State the blood parasite species.
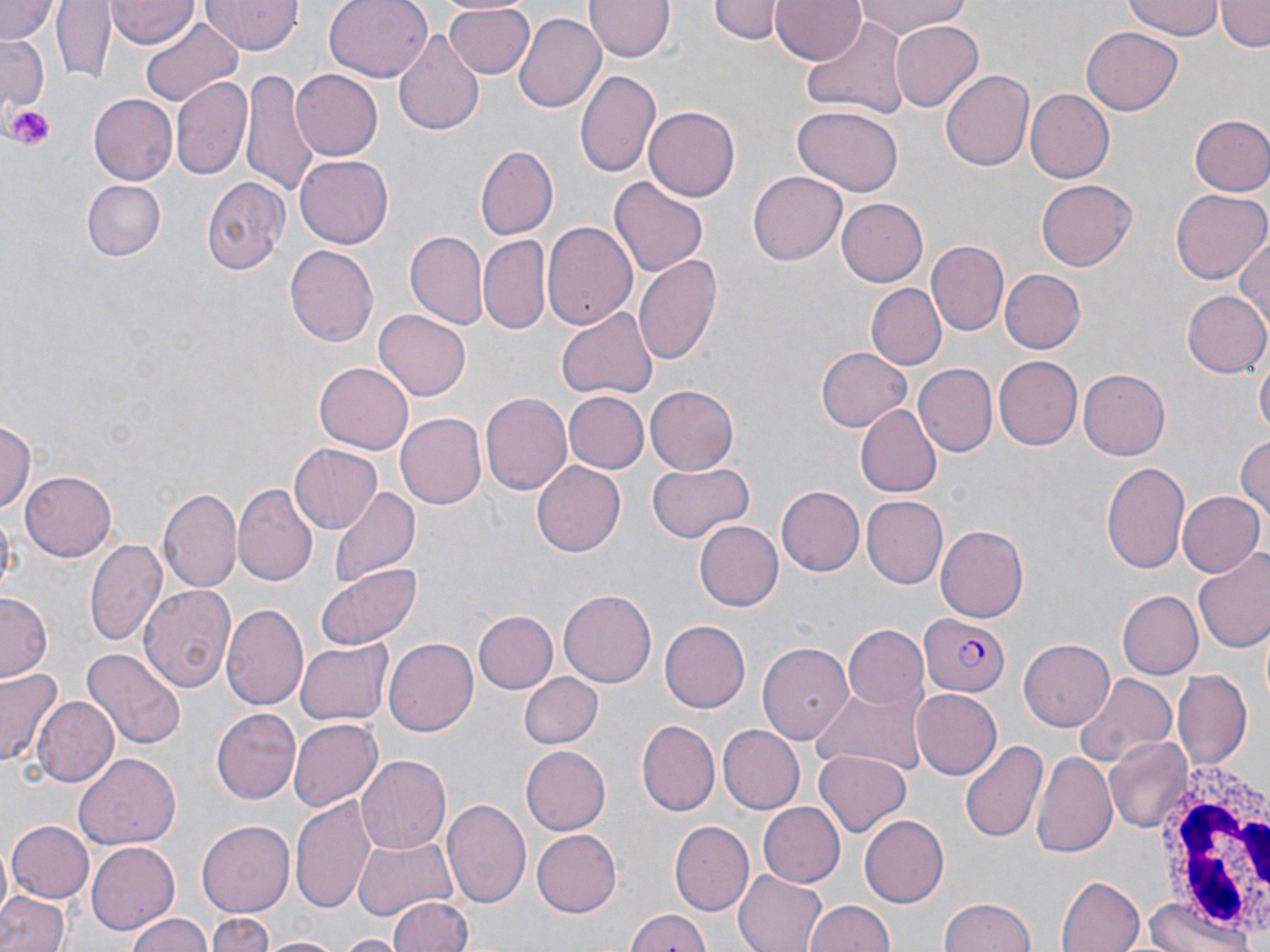
Plasmodium falciparum.

{
  "modality": "light microscopy",
  "white_blood_cell_locations": "approximate bounding boxes as [x1, y1, x2, y2] in pixels: [1149, 755, 1270, 944]",
  "image_size": "1270×952 pixels",
  "preparation": "thin blood film",
  "stain": "May-Grünwald-Giemsa",
  "platelet_locations": "approximate bounding boxes as [x1, y1, x2, y2] in pixels: [6, 103, 56, 148]",
  "magnification": "1000x",
  "field_of_view": "one of a larger specimen",
  "plasmodium_falciparum_infected_red_blood_cell_locations": "approximate bounding boxes as [x1, y1, x2, y2] in pixels: [920, 612, 1012, 698]",
  "uninfected_red_blood_cell_locations": "approximate bounding boxes as [x1, y1, x2, y2] in pixels: [0, 0, 61, 45], [51, 0, 115, 84], [198, 0, 305, 56], [325, 0, 433, 81], [584, 0, 671, 61], [712, 0, 779, 44], [770, 0, 862, 65], [852, 0, 969, 38], [1122, 0, 1224, 40], [1218, 0, 1269, 52], [107, 2, 196, 48], [443, 4, 533, 77], [513, 11, 605, 113], [137, 15, 243, 107], [803, 16, 911, 119], [890, 21, 984, 111], [1083, 26, 1183, 113], [392, 28, 483, 137], [0, 35, 48, 114], [242, 68, 320, 203], [575, 68, 661, 180], [940, 68, 1035, 171], [291, 69, 383, 160], [171, 74, 254, 180], [1025, 89, 1114, 183], [89, 93, 177, 185], [790, 105, 903, 196], [644, 106, 739, 201], [1188, 114, 1270, 198], [476, 146, 558, 240], [295, 155, 392, 248], [748, 172, 846, 265], [202, 175, 290, 276], [610, 176, 707, 276], [1035, 178, 1138, 271], [81, 179, 165, 261], [1170, 189, 1267, 285], [837, 197, 928, 288], [541, 217, 638, 331], [406, 230, 485, 330], [1234, 233, 1269, 340], [479, 236, 550, 333], [927, 241, 1007, 334], [285, 243, 378, 349], [633, 254, 722, 369], [999, 269, 1084, 354], [867, 283, 946, 369], [1182, 291, 1270, 378], [556, 306, 658, 401], [373, 309, 470, 403], [816, 347, 912, 432], [994, 354, 1082, 450], [1256, 355, 1269, 440], [314, 361, 414, 453], [914, 364, 997, 456], [1079, 369, 1170, 460], [645, 385, 738, 473], [480, 391, 573, 495], [565, 392, 649, 474], [854, 404, 941, 499], [396, 414, 485, 509], [0, 417, 35, 518], [1234, 431, 1269, 532], [289, 444, 382, 533], [1100, 459, 1191, 574], [646, 460, 754, 546], [532, 462, 625, 558], [20, 470, 116, 561], [234, 484, 318, 589], [156, 486, 241, 593], [328, 486, 419, 590], [776, 486, 863, 577], [1175, 489, 1263, 579], [862, 496, 948, 587], [693, 519, 782, 611], [936, 524, 1028, 622], [85, 538, 167, 647], [1194, 551, 1270, 656], [315, 563, 422, 650], [138, 583, 237, 692], [558, 588, 657, 688], [1118, 590, 1203, 678], [1, 591, 54, 684], [219, 604, 308, 713], [473, 611, 556, 694], [659, 620, 749, 713], [842, 625, 927, 710], [384, 635, 479, 737], [1021, 638, 1115, 730], [296, 639, 392, 725], [758, 641, 853, 747], [80, 647, 187, 749], [0, 667, 62, 770], [1172, 671, 1252, 771], [517, 672, 603, 750], [1073, 674, 1176, 766], [814, 681, 925, 774], [912, 689, 1002, 779], [31, 695, 118, 789], [212, 708, 300, 804], [289, 718, 383, 811], [637, 720, 718, 816], [718, 723, 806, 813], [1105, 736, 1192, 832], [961, 737, 1047, 844], [518, 745, 609, 836], [1032, 748, 1117, 861], [815, 749, 913, 835], [74, 751, 182, 849], [356, 756, 451, 855], [289, 792, 377, 913], [441, 798, 531, 911], [757, 802, 844, 887], [859, 816, 948, 906], [197, 819, 294, 919], [669, 820, 754, 916], [7, 821, 94, 902], [531, 829, 622, 917], [354, 834, 457, 920], [86, 841, 179, 935], [735, 869, 829, 952], [1056, 876, 1144, 952], [0, 892, 69, 952], [388, 894, 472, 952], [1144, 896, 1256, 952], [940, 897, 1039, 952], [803, 898, 894, 952], [623, 907, 712, 952], [123, 912, 216, 952], [208, 914, 275, 952], [339, 934, 402, 952], [261, 936, 344, 952]"
}